Locate and identify every blood parasite.
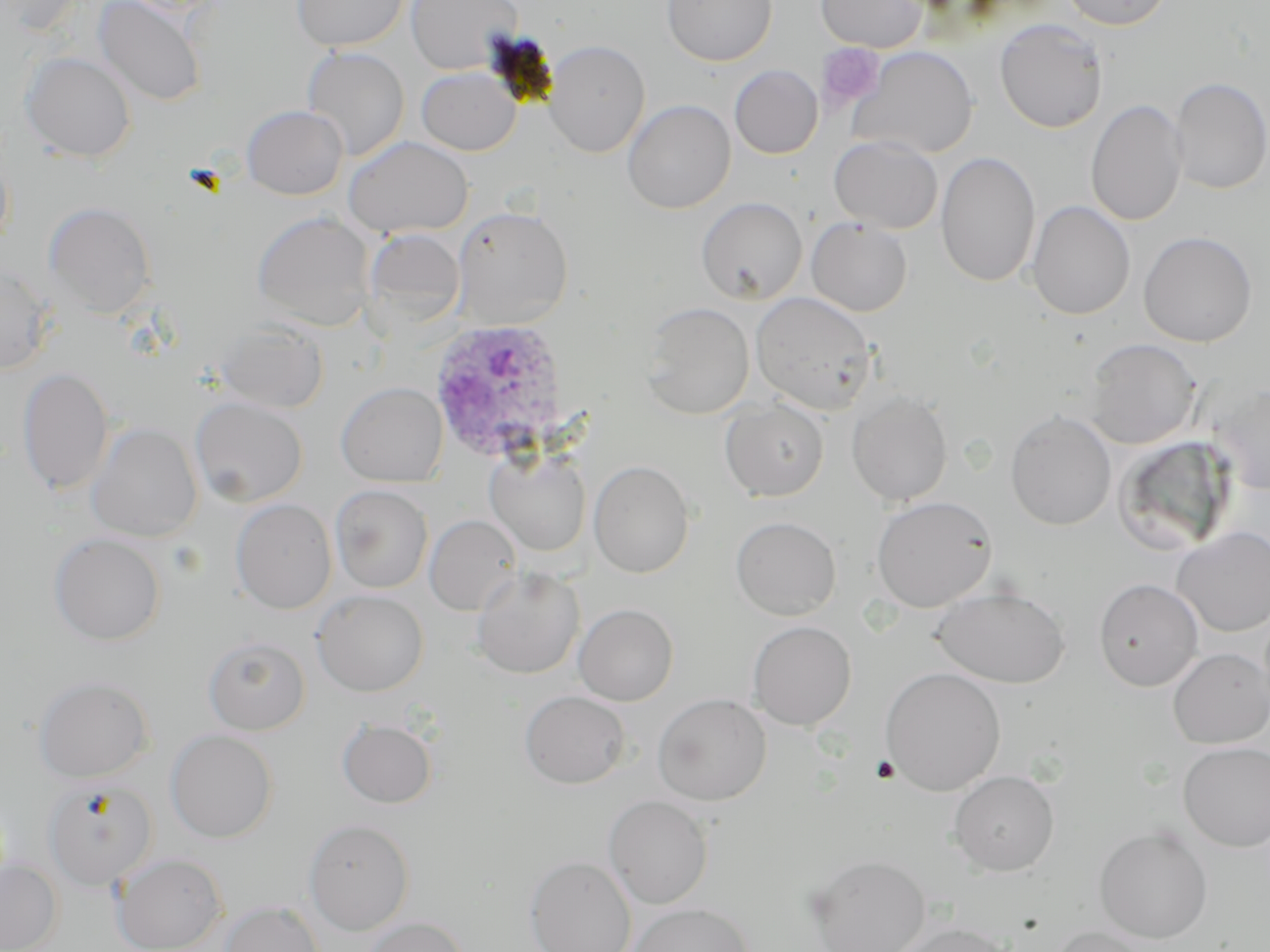
Approximate bounding boxes as [x1, y1, x2, y2] in pixels.
Plasmodium ovale-infected red blood cells: [428, 317, 569, 462].
No Plasmodium falciparum, Plasmodium malariae, Plasmodium vivax, Babesia divergens, or Trypanosoma brucei observed.

Uninfected red blood cell locations: [93, 0, 206, 106], [292, 0, 409, 51], [405, 0, 522, 74], [662, 0, 777, 66], [816, 0, 926, 52], [1058, 0, 1173, 30], [994, 18, 1108, 133], [543, 40, 650, 157], [301, 46, 409, 162], [850, 46, 978, 159], [20, 52, 136, 162], [729, 65, 823, 159], [416, 67, 521, 155], [1168, 77, 1269, 195], [621, 99, 735, 213], [1086, 99, 1188, 227], [242, 105, 348, 200], [829, 135, 943, 234], [343, 136, 473, 238], [936, 151, 1041, 287], [0, 156, 13, 255], [696, 196, 808, 304], [1027, 200, 1135, 320], [44, 202, 157, 319], [451, 206, 573, 328], [251, 211, 376, 331], [806, 217, 913, 317], [362, 228, 466, 329], [1138, 231, 1257, 347], [0, 263, 56, 374], [750, 291, 877, 414], [641, 302, 755, 419], [217, 322, 329, 414], [1084, 338, 1201, 449], [17, 367, 114, 496], [1208, 381, 1269, 495], [336, 382, 448, 487], [846, 389, 953, 506], [190, 396, 308, 507], [721, 399, 829, 501], [1006, 411, 1117, 531], [87, 422, 203, 542], [1112, 436, 1238, 557], [485, 448, 592, 557], [589, 460, 695, 578], [330, 485, 433, 593], [871, 495, 998, 612], [231, 498, 337, 614], [424, 514, 522, 615], [731, 516, 841, 621], [1171, 527, 1270, 637], [49, 533, 166, 645], [471, 567, 584, 678], [1094, 578, 1203, 692], [932, 586, 1070, 688], [312, 589, 429, 696], [573, 603, 679, 706], [747, 620, 856, 730], [203, 636, 311, 735], [1167, 648, 1270, 749], [880, 667, 1005, 795], [34, 675, 154, 782], [520, 690, 630, 788], [652, 693, 771, 805], [337, 718, 437, 808], [166, 729, 278, 843], [1178, 741, 1270, 852], [948, 770, 1059, 875], [44, 778, 157, 891], [603, 795, 713, 909], [303, 819, 415, 936], [1094, 826, 1214, 944], [112, 852, 227, 952], [806, 854, 931, 952], [525, 855, 637, 952], [0, 859, 62, 952], [219, 901, 324, 952], [627, 901, 755, 952], [360, 916, 469, 952], [894, 921, 1014, 952], [1047, 925, 1153, 952]. Platelet locations: [816, 43, 884, 111], [869, 755, 901, 784]. Slide-level diagnosis: Plasmodium ovale. Thin blood smear. Light microscopy. Image is 1270×952 pixels. Captured at 1000x magnification. May-Grünwald-Giemsa-stained preparation. Single field of view.